Outline each uninfected red blood cell.
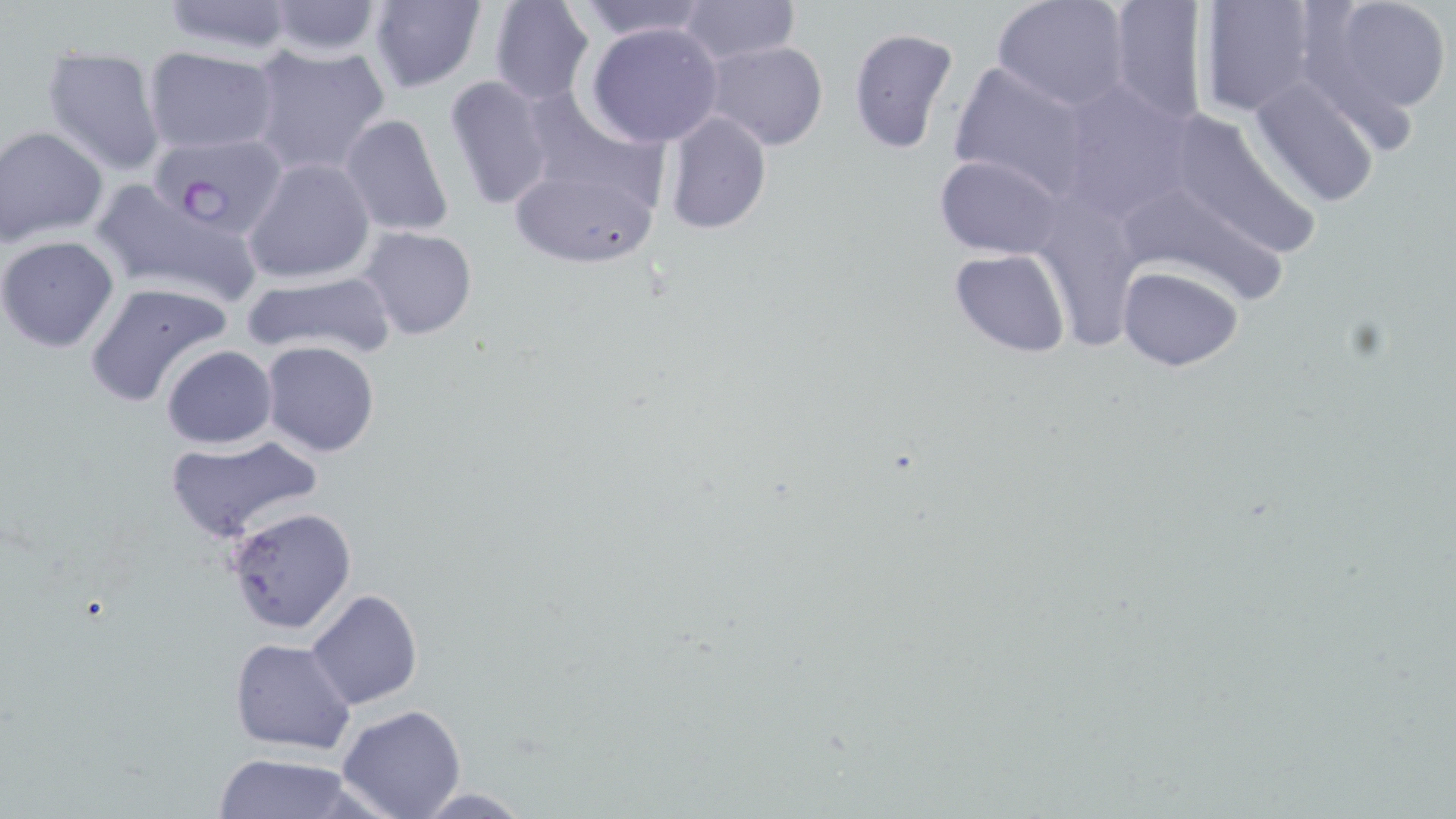

Approximate bounding boxes as (x1, y1, x2, y2) in pixels.
Uninfected red blood cells: (153, 0, 302, 58), (368, 0, 488, 94), (488, 0, 596, 106), (573, 0, 716, 42), (677, 0, 800, 66), (1103, 0, 1211, 127), (1194, 0, 1316, 117), (1310, 0, 1453, 121), (261, 1, 387, 58), (992, 1, 1133, 112), (584, 21, 724, 147), (846, 26, 959, 155), (702, 40, 831, 152), (246, 42, 392, 178), (40, 43, 167, 176), (142, 47, 280, 156), (946, 58, 1094, 198), (442, 74, 555, 211), (1247, 74, 1387, 208), (1055, 78, 1197, 219), (520, 83, 674, 210), (1160, 106, 1321, 263), (662, 111, 771, 233), (339, 113, 454, 238), (1, 126, 107, 246), (508, 153, 665, 270), (935, 154, 1065, 260), (243, 158, 376, 285), (90, 179, 266, 305), (1131, 197, 1287, 304), (1043, 201, 1146, 358), (358, 225, 479, 342), (0, 236, 120, 353), (948, 249, 1073, 358), (1117, 265, 1244, 372), (240, 269, 396, 362), (83, 281, 233, 408), (260, 341, 381, 458), (162, 344, 277, 448), (164, 433, 325, 542), (223, 505, 358, 635), (305, 589, 422, 709), (229, 637, 357, 754), (336, 704, 467, 819), (209, 752, 369, 819), (408, 787, 537, 817).

Plasmodium falciparum-infected red blood cell locations: (153, 134, 285, 234). Slide-level diagnosis: Plasmodium falciparum. Single field of view. Captured at 1000x magnification. Image is 1456×819 pixels. Optical microscopy. Thin blood film. May-Grünwald-Giemsa stain.